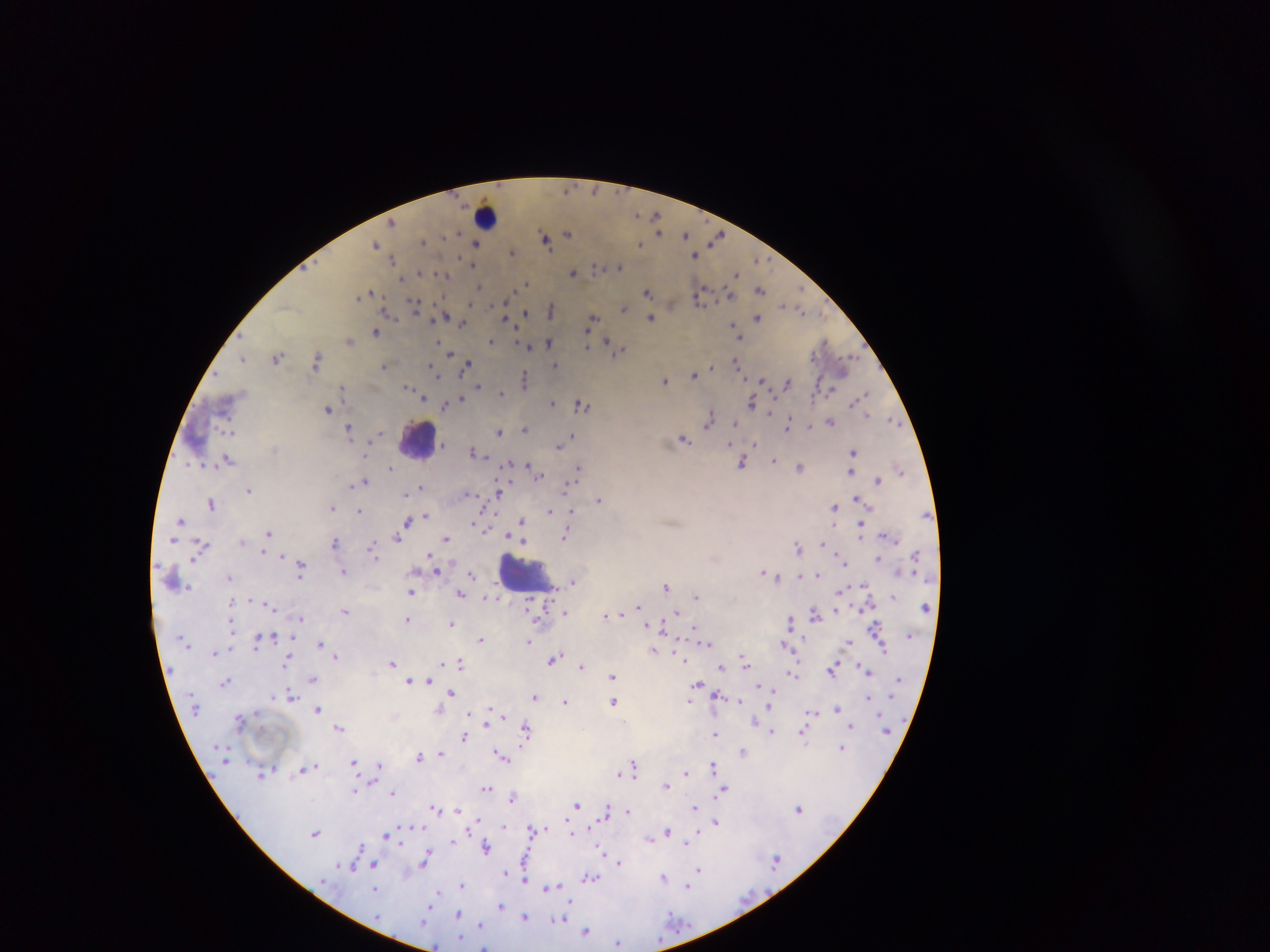
Approximate centers as (x, y) in pixels.
Summary:
  - Plasmodium parasite locations: (656, 216), (392, 223), (659, 232), (458, 233), (568, 234), (686, 235), (718, 236), (545, 238), (423, 241), (376, 243), (476, 244), (639, 244), (512, 253), (694, 255), (393, 259), (474, 265), (619, 266), (596, 267), (420, 272), (572, 273), (737, 274), (444, 276), (402, 280), (526, 283), (478, 286), (523, 286), (760, 289), (648, 291), (367, 294), (730, 295), (359, 296), (702, 298), (414, 305), (670, 305), (783, 305), (624, 308), (551, 310), (387, 311), (803, 311), (526, 313), (445, 315), (650, 318), (757, 318), (592, 319), (507, 320), (462, 323), (734, 327), (376, 333), (738, 334), (739, 337), (349, 341), (491, 341), (439, 342), (606, 342), (825, 342), (548, 343), (587, 345), (611, 346), (528, 347), (618, 351), (450, 354), (278, 357), (243, 358), (316, 360), (737, 361), (554, 364), (467, 365), (383, 366), (712, 368), (433, 370), (439, 375), (694, 376), (525, 378), (665, 381), (762, 381), (787, 382), (478, 386), (407, 387), (343, 389), (502, 394), (861, 397), (424, 398), (461, 399), (457, 402), (553, 403), (752, 403), (582, 404), (446, 406), (327, 409), (771, 412), (867, 415), (709, 419), (893, 421), (831, 422), (736, 424), (788, 424), (228, 429), (524, 429), (349, 430), (499, 432), (572, 435), (685, 440), (729, 442), (755, 444), (558, 447), (473, 451), (854, 452), (227, 459), (773, 461), (742, 463), (528, 466), (800, 467), (391, 468), (579, 469), (900, 469), (851, 472), (538, 473), (878, 480), (363, 482), (421, 486), (566, 487), (249, 490), (499, 493), (406, 494), (857, 499), (599, 500), (211, 503), (834, 506), (332, 507), (359, 511), (549, 511), (572, 512), (426, 516), (414, 519), (180, 520), (521, 520), (408, 522), (477, 525), (861, 525), (269, 532), (398, 536), (564, 536), (266, 538), (446, 539), (173, 540), (334, 542), (824, 544), (202, 545), (797, 546), (373, 548), (263, 552), (840, 554), (282, 555), (879, 558), (301, 569), (436, 570), (344, 571), (765, 573), (818, 574), (472, 575), (777, 576), (229, 577), (573, 582), (865, 584), (666, 587), (411, 592), (460, 593), (696, 596), (487, 598), (272, 606), (639, 607), (836, 609), (345, 611), (565, 613), (815, 613), (622, 614), (677, 614), (606, 615), (301, 618), (407, 620), (789, 621), (452, 624), (876, 627), (232, 628), (696, 628), (273, 637), (480, 639), (257, 641), (529, 641), (849, 642), (706, 643), (319, 644), (784, 645), (884, 647), (653, 649), (215, 652), (335, 656), (554, 659), (682, 659), (287, 662), (745, 662), (393, 663), (461, 663), (442, 664), (581, 666), (721, 667), (833, 669), (868, 670), (792, 674), (612, 677), (313, 679), (409, 680), (225, 681), (613, 682), (696, 684), (760, 686), (451, 693), (290, 695), (717, 695), (534, 696), (868, 697), (690, 700), (739, 701), (565, 702), (614, 702), (838, 708), (317, 709), (811, 712), (239, 720), (851, 726), (339, 728), (526, 729), (772, 732), (803, 732), (716, 734), (464, 737), (842, 748), (743, 751), (440, 754), (501, 756), (419, 757), (355, 762), (714, 765), (380, 766), (311, 767), (635, 768), (303, 769), (686, 772), (262, 773), (619, 773), (666, 785), (486, 788), (356, 791), (722, 791), (392, 792), (513, 797), (577, 805), (695, 807), (434, 808), (606, 808), (799, 808), (457, 810), (628, 811), (476, 819), (716, 822), (504, 828), (533, 830), (667, 832), (315, 833), (389, 834), (650, 838), (686, 842), (485, 847), (601, 849), (426, 858), (619, 862), (373, 864), (352, 866), (524, 868), (699, 869), (506, 874), (524, 876), (591, 877), (664, 877), (461, 885), (688, 887), (550, 888), (375, 889), (436, 894), (500, 905), (458, 914), (524, 917), (561, 919), (480, 925), (586, 931), (618, 943), (435, 946), (483, 946)
  - Leukocyte locations: (487, 215), (418, 441), (524, 573)
  - Preparation: thick blood film
  - Country: Ghana
  - Capture: mobile-phone photograph through a microscope
  - Image size: 1270×952 pixels
  - Field of view: single